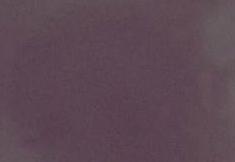
1000x magnification. Micrograph. An erythrocyte is shown.